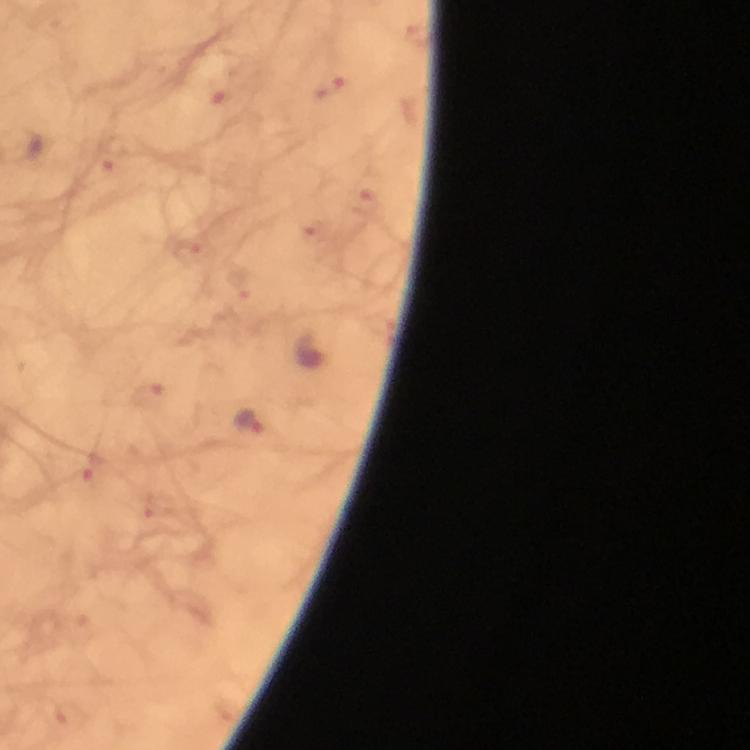
Approximate centers as {x, y} in pixels.
Summary:
  - Plasmodium parasite locations: {330, 89}, {222, 94}, {110, 163}, {363, 202}, {188, 253}, {149, 395}, {250, 418}, {94, 469}
  - Magnification: 100x
  - Image size: 750×750 pixels
  - Context: from a malaria diagnostic workup
  - Preparation: thick blood film
  - Immersion oil: applied
  - Stain: Giemsa
  - Cropped from: a single field of view
  - Capture: smartphone photograph through a microscope